Give the extent of all Plasmodium ovale-infected red blood cells.
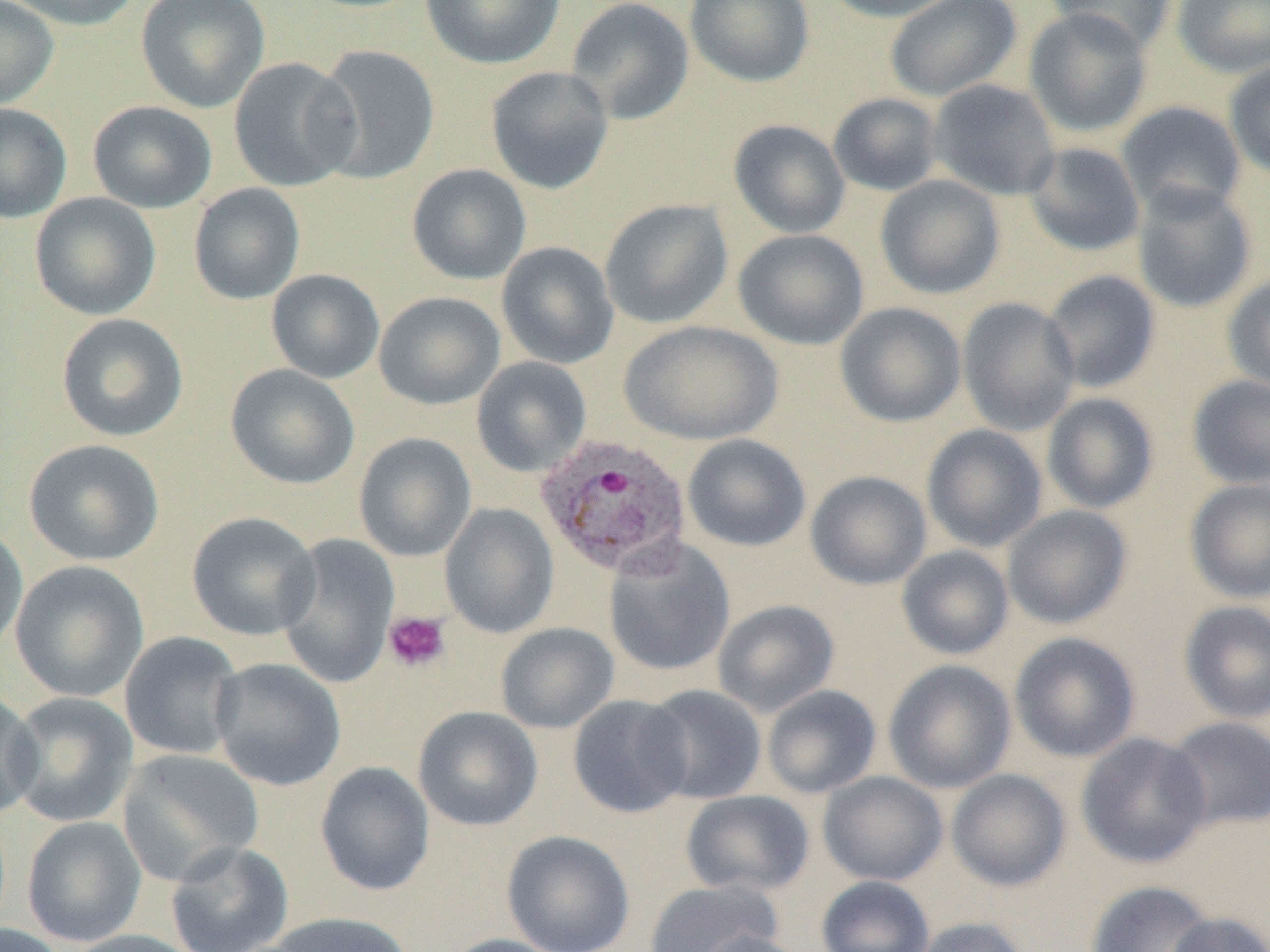
Approximate bounding boxes as (x1, y1, x2, y2) in pixels.
Plasmodium ovale-infected red blood cells: (535, 433, 693, 579).

{
  "slide_level_diagnosis": "Plasmodium ovale",
  "magnification": "1000x",
  "modality": "light microscopy",
  "platelet_locations": "approximate bounding boxes as (x1, y1, x2, y2) in pixels: (383, 611, 450, 673)",
  "image_size": "1270×952 pixels",
  "preparation": "thin blood film",
  "uninfected_red_blood_cell_locations": "approximate bounding boxes as (x1, y1, x2, y2) in pixels: (4, 0, 141, 31), (136, 0, 270, 113), (419, 0, 566, 70), (566, 0, 695, 125), (685, 0, 815, 87), (820, 0, 963, 22), (884, 0, 1023, 102), (1044, 0, 1176, 54), (1172, 0, 1270, 78), (0, 1, 59, 111), (1023, 7, 1153, 139), (312, 44, 440, 184), (228, 56, 361, 192), (1224, 59, 1270, 180), (485, 66, 614, 195), (928, 78, 1061, 201), (828, 92, 943, 196), (88, 100, 218, 213), (1116, 101, 1247, 218), (0, 103, 72, 224), (728, 119, 851, 239), (1024, 142, 1145, 257), (407, 164, 531, 284), (875, 174, 1005, 300), (1131, 182, 1257, 315), (188, 183, 305, 305), (29, 193, 161, 320), (599, 199, 734, 329), (733, 229, 869, 350), (496, 241, 619, 370), (266, 269, 385, 383), (1041, 269, 1161, 394), (1223, 271, 1270, 395), (373, 292, 505, 410), (957, 297, 1080, 437), (835, 302, 967, 428), (56, 313, 189, 442), (619, 320, 783, 446), (471, 357, 592, 477), (225, 364, 359, 489), (1186, 374, 1270, 490), (1041, 392, 1160, 514), (921, 424, 1048, 553), (353, 432, 477, 562), (681, 433, 811, 552), (23, 439, 164, 566), (805, 471, 932, 590), (1184, 478, 1270, 604), (440, 503, 559, 638), (1002, 505, 1133, 630), (187, 511, 321, 640), (0, 522, 29, 658), (276, 533, 400, 689), (603, 539, 736, 678), (896, 545, 1014, 660), (9, 560, 149, 702), (712, 599, 840, 717), (1178, 600, 1270, 724), (495, 622, 619, 734), (119, 631, 244, 760), (1009, 631, 1141, 763), (209, 657, 346, 792), (882, 659, 1017, 794), (641, 684, 767, 805), (762, 685, 882, 799), (0, 687, 43, 821), (5, 692, 138, 827), (568, 694, 693, 818), (413, 706, 544, 831), (1163, 716, 1270, 832), (1075, 732, 1212, 869), (117, 748, 265, 885), (315, 761, 435, 896), (946, 769, 1071, 891), (818, 772, 948, 886), (679, 790, 815, 897), (21, 816, 146, 947), (501, 830, 635, 952), (164, 840, 294, 952), (816, 875, 935, 952), (643, 878, 784, 952), (1084, 880, 1217, 952), (264, 911, 414, 952), (1165, 912, 1270, 952), (907, 917, 1030, 952), (0, 923, 69, 952), (61, 929, 206, 952), (691, 930, 816, 952), (439, 934, 567, 952)",
  "field_of_view": "single"
}